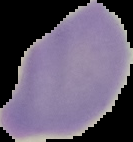

Summary:
  - Image type: segmented cell region on a black background
  - Image size: 133×142 pixels
  - Malaria status: uninfected
  - Preparation: thin blood smear